Give the position of every leukocyte visible.
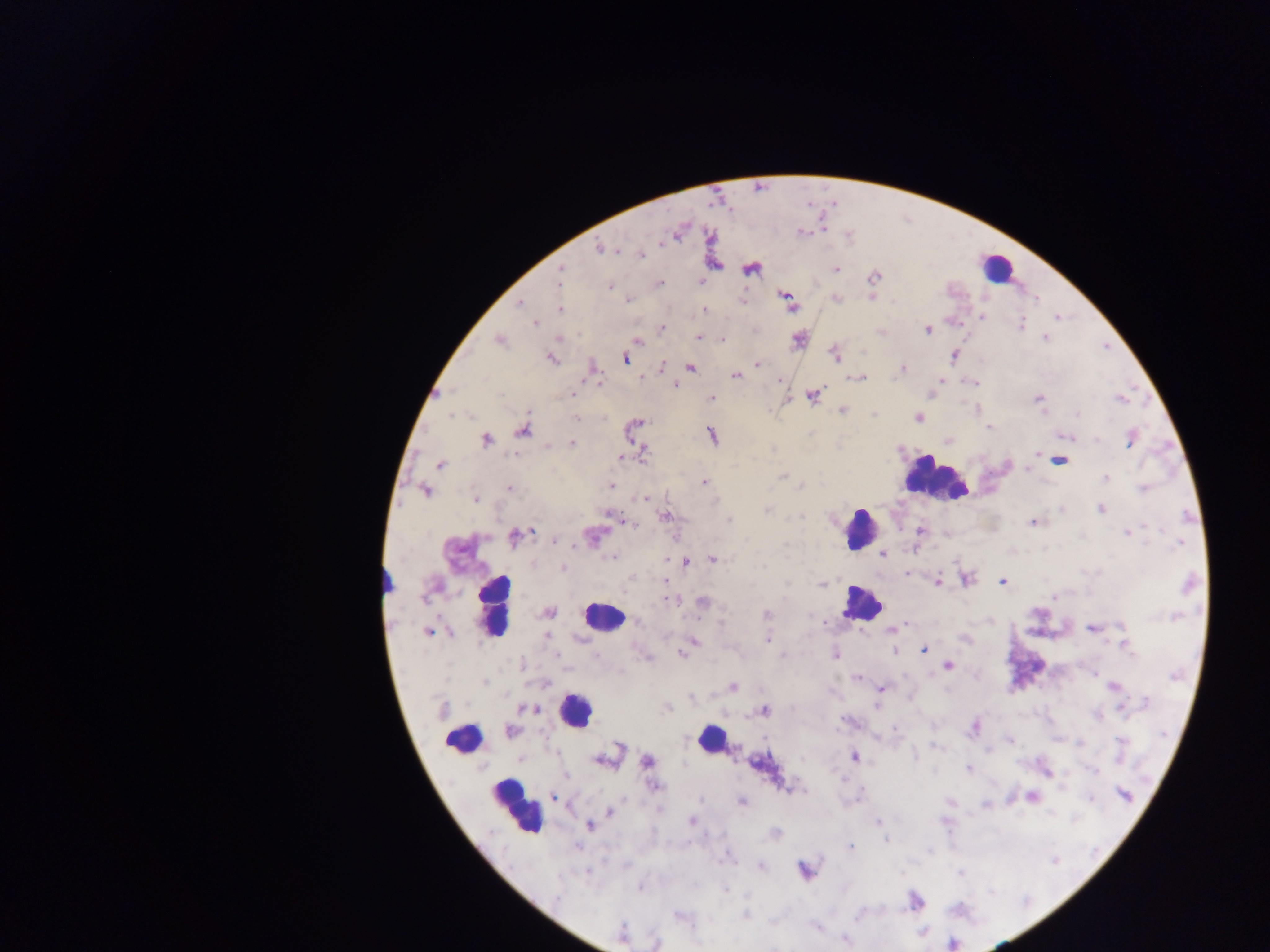
Approximate centers as [x, y] in pixels.
Leukocytes: [996, 268], [935, 477], [859, 528], [861, 602], [492, 607], [601, 616], [574, 709], [710, 738], [463, 739], [516, 806].

malaria parasite locations = approximate centers as [x, y] in pixels: [678, 231], [600, 248], [641, 255], [750, 268], [835, 269], [560, 270], [873, 276], [658, 282], [609, 286], [870, 296], [835, 298], [628, 299], [786, 301], [521, 303], [559, 309], [704, 309], [981, 317], [1057, 317], [535, 322], [1020, 325], [662, 328], [927, 330], [698, 337], [1044, 337], [798, 338], [499, 339], [721, 339], [637, 340], [835, 353], [954, 355], [550, 358], [625, 358], [757, 364], [690, 366], [592, 367], [661, 368], [902, 369], [734, 375], [859, 378], [941, 379], [974, 382], [598, 383], [675, 384], [571, 393], [812, 395], [1038, 398], [712, 399], [1121, 399], [842, 409], [575, 417], [917, 417], [636, 423], [989, 426], [522, 431], [711, 434], [1068, 436], [485, 439], [1131, 439], [948, 441], [571, 443], [642, 451], [1037, 452], [622, 457], [1058, 460], [440, 464], [1029, 470], [782, 476], [1106, 478], [703, 482], [610, 486], [509, 488], [1143, 489], [425, 491], [645, 497], [476, 498], [1100, 508], [664, 516], [621, 520], [1034, 521], [919, 530], [1129, 533], [515, 535], [592, 535], [554, 540], [882, 554], [615, 558], [713, 558], [685, 560], [562, 568], [907, 574], [965, 578], [663, 581], [937, 581], [1002, 581], [821, 582], [1053, 596], [668, 599], [702, 603], [547, 612], [766, 614], [638, 620], [907, 624], [1093, 627], [892, 629], [428, 631], [547, 635], [768, 639], [693, 641], [1125, 643], [923, 649], [893, 651], [681, 653], [836, 654], [947, 665], [857, 677], [1113, 686], [732, 687], [881, 688], [525, 708], [668, 708], [441, 709], [764, 710], [973, 727], [510, 731], [1010, 740], [607, 755], [853, 756], [648, 762], [969, 769], [1046, 771], [653, 785], [790, 788], [1032, 796], [1125, 796], [553, 797], [741, 801], [950, 802], [986, 805], [610, 811], [692, 821], [876, 821], [589, 825], [775, 833], [885, 838], [851, 846], [760, 866], [804, 869], [640, 887], [915, 900], [622, 935], [844, 939], [656, 943]
preparation = thick blood smear
capture = mobile-phone photograph through a microscope
image size = 1270×952 pixels
field of view = single
country = Ghana